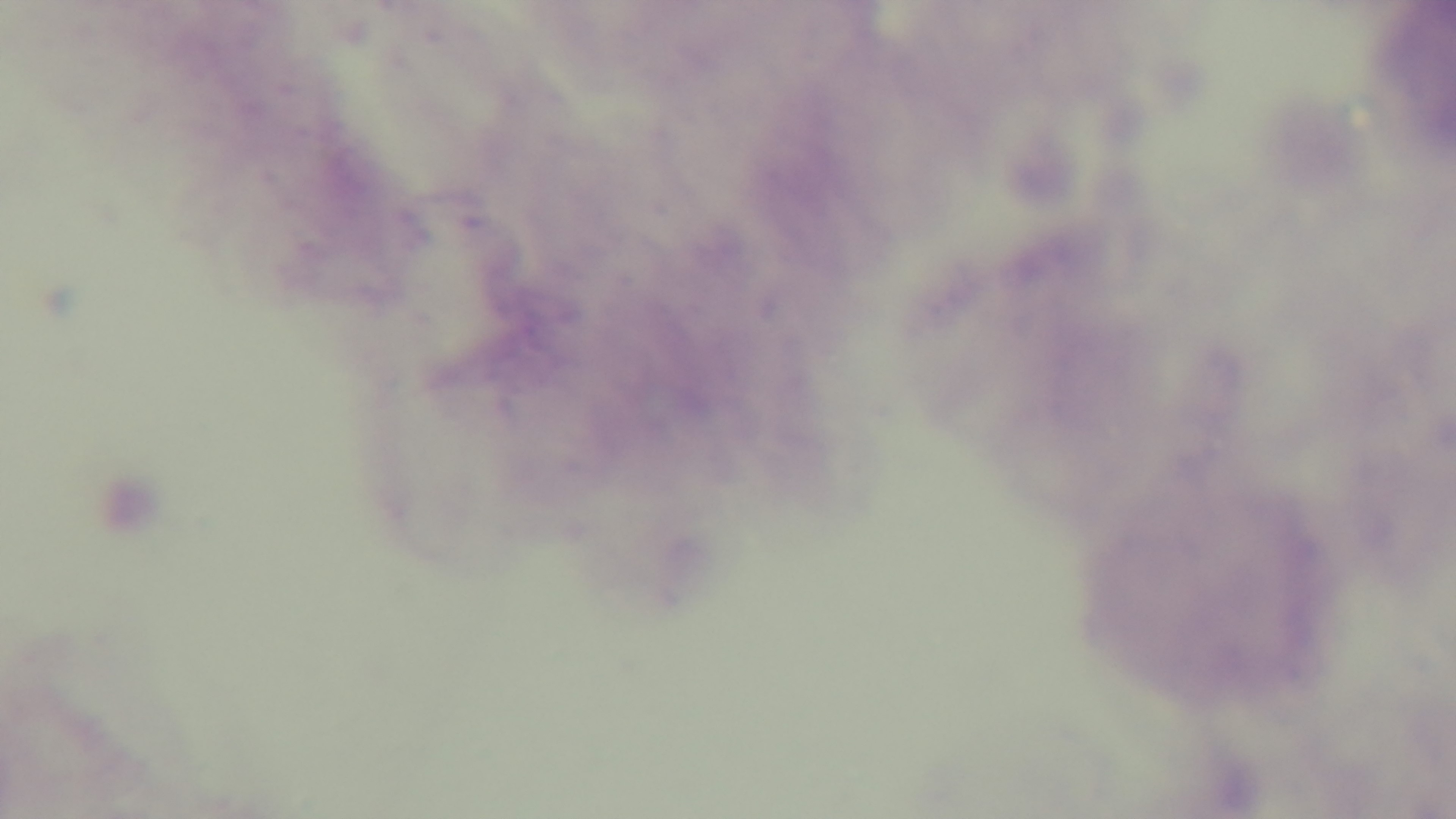

Giemsa-stained. Preparation: thick smear. Malaria status: uninfected. Oil-immersion objective, 100x. Mounted 4K digital camera. One field from the slide. Light microscopy.